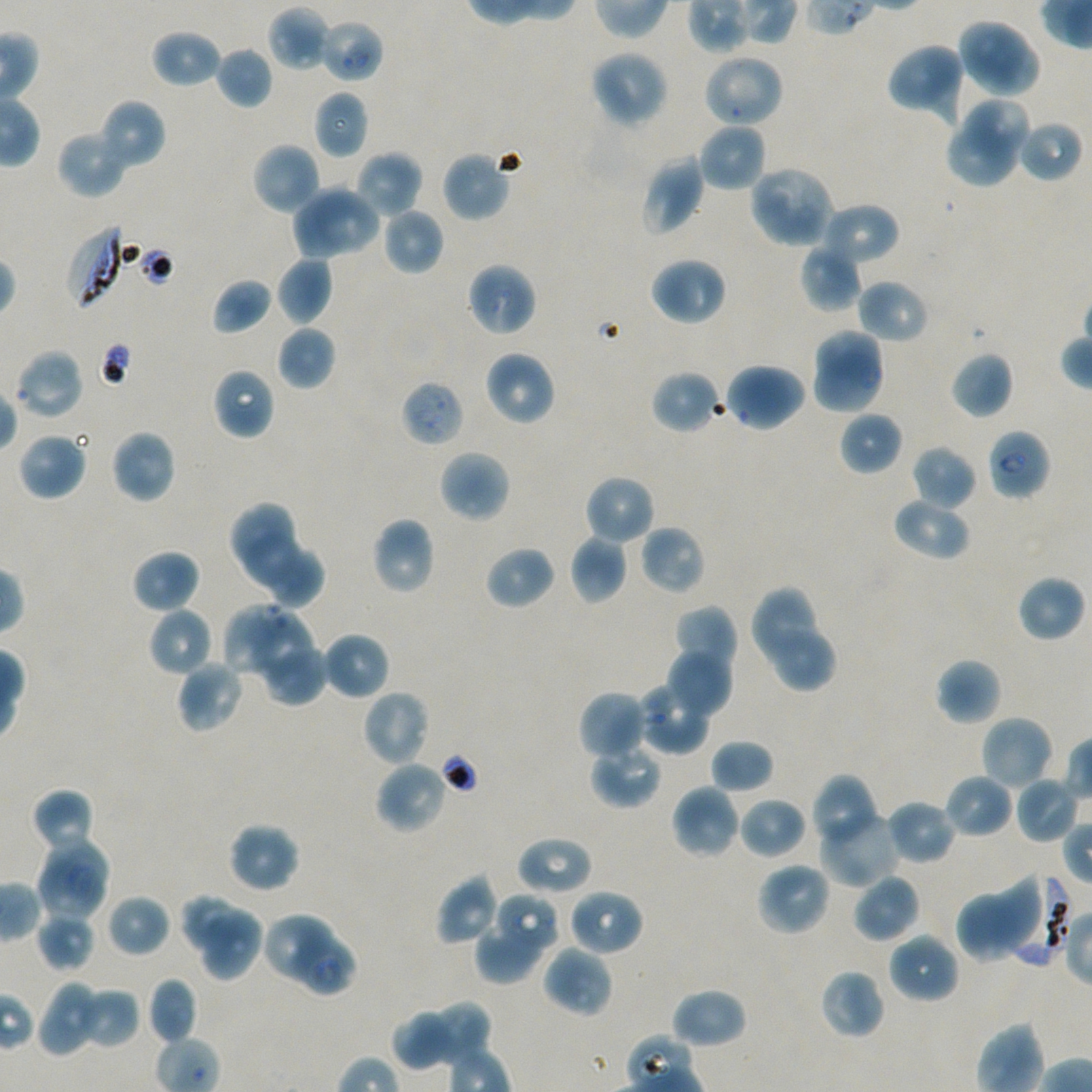
Approximate bounding rectangles given as corner coordinates in pixels from the top-left. Not every red blood cell is marked. A life-cycle stage — or a range of stages, where the recorded stages span more than one — follows each staged infected red blood cell.
Summary:
  - Locations of uninfected red blood cells: (x1=266, y1=6, x2=330, y2=72), (x1=957, y1=16, x2=1027, y2=88), (x1=150, y1=29, x2=221, y2=88), (x1=971, y1=37, x2=1038, y2=98), (x1=886, y1=42, x2=966, y2=121), (x1=215, y1=46, x2=273, y2=109), (x1=589, y1=49, x2=670, y2=129), (x1=701, y1=54, x2=785, y2=128), (x1=313, y1=90, x2=369, y2=160), (x1=98, y1=98, x2=166, y2=170), (x1=963, y1=102, x2=1030, y2=158), (x1=1016, y1=120, x2=1083, y2=184), (x1=697, y1=122, x2=767, y2=192), (x1=947, y1=126, x2=1017, y2=187), (x1=56, y1=129, x2=131, y2=199), (x1=252, y1=142, x2=321, y2=216), (x1=441, y1=150, x2=512, y2=222), (x1=354, y1=151, x2=422, y2=219), (x1=640, y1=154, x2=705, y2=236), (x1=748, y1=164, x2=836, y2=249), (x1=295, y1=179, x2=354, y2=260), (x1=315, y1=185, x2=382, y2=253), (x1=818, y1=202, x2=900, y2=268), (x1=381, y1=207, x2=444, y2=275), (x1=800, y1=240, x2=863, y2=312), (x1=276, y1=255, x2=333, y2=326), (x1=649, y1=256, x2=728, y2=326), (x1=467, y1=261, x2=537, y2=338), (x1=212, y1=278, x2=272, y2=335), (x1=856, y1=278, x2=930, y2=344), (x1=276, y1=325, x2=336, y2=390), (x1=813, y1=329, x2=883, y2=384), (x1=14, y1=348, x2=84, y2=420), (x1=483, y1=350, x2=556, y2=426), (x1=812, y1=350, x2=886, y2=416), (x1=950, y1=351, x2=1013, y2=419), (x1=724, y1=362, x2=807, y2=433), (x1=212, y1=367, x2=275, y2=441), (x1=651, y1=369, x2=724, y2=434), (x1=839, y1=410, x2=903, y2=476), (x1=110, y1=428, x2=177, y2=503), (x1=17, y1=431, x2=89, y2=501), (x1=912, y1=445, x2=977, y2=510), (x1=438, y1=449, x2=511, y2=523), (x1=583, y1=474, x2=655, y2=545), (x1=892, y1=496, x2=972, y2=560), (x1=228, y1=503, x2=293, y2=564), (x1=371, y1=516, x2=437, y2=595), (x1=639, y1=525, x2=706, y2=596), (x1=242, y1=531, x2=304, y2=587), (x1=569, y1=534, x2=629, y2=604), (x1=485, y1=545, x2=556, y2=609), (x1=131, y1=548, x2=202, y2=613), (x1=271, y1=549, x2=325, y2=611), (x1=1016, y1=575, x2=1085, y2=642), (x1=749, y1=586, x2=817, y2=663), (x1=223, y1=604, x2=286, y2=674), (x1=673, y1=604, x2=738, y2=672), (x1=147, y1=606, x2=214, y2=677), (x1=255, y1=613, x2=314, y2=679), (x1=322, y1=631, x2=390, y2=699), (x1=776, y1=632, x2=837, y2=689), (x1=666, y1=647, x2=732, y2=718), (x1=266, y1=648, x2=328, y2=706), (x1=935, y1=657, x2=1002, y2=725), (x1=175, y1=659, x2=245, y2=734), (x1=637, y1=684, x2=711, y2=755), (x1=361, y1=689, x2=431, y2=767), (x1=577, y1=689, x2=649, y2=762), (x1=980, y1=715, x2=1055, y2=792), (x1=710, y1=739, x2=774, y2=793), (x1=593, y1=746, x2=660, y2=807), (x1=374, y1=760, x2=449, y2=835), (x1=810, y1=774, x2=873, y2=840), (x1=943, y1=774, x2=1014, y2=839), (x1=1015, y1=775, x2=1078, y2=843), (x1=670, y1=784, x2=741, y2=860), (x1=31, y1=788, x2=96, y2=856), (x1=739, y1=797, x2=808, y2=860), (x1=885, y1=799, x2=958, y2=864), (x1=820, y1=807, x2=900, y2=887), (x1=228, y1=821, x2=300, y2=893), (x1=46, y1=835, x2=107, y2=899), (x1=516, y1=835, x2=594, y2=896), (x1=756, y1=862, x2=832, y2=937), (x1=36, y1=864, x2=107, y2=922), (x1=852, y1=873, x2=922, y2=943), (x1=435, y1=874, x2=500, y2=946), (x1=956, y1=877, x2=1044, y2=962), (x1=568, y1=888, x2=644, y2=956), (x1=107, y1=894, x2=171, y2=957), (x1=500, y1=896, x2=557, y2=947), (x1=182, y1=897, x2=249, y2=949), (x1=200, y1=908, x2=260, y2=982), (x1=36, y1=913, x2=95, y2=971), (x1=267, y1=916, x2=333, y2=979), (x1=479, y1=922, x2=542, y2=983), (x1=888, y1=932, x2=960, y2=1004), (x1=289, y1=936, x2=358, y2=996), (x1=543, y1=945, x2=613, y2=1017), (x1=819, y1=968, x2=885, y2=1039), (x1=147, y1=977, x2=198, y2=1045), (x1=37, y1=979, x2=103, y2=1057), (x1=79, y1=987, x2=139, y2=1049), (x1=670, y1=987, x2=748, y2=1049), (x1=435, y1=998, x2=490, y2=1070), (x1=392, y1=1011, x2=448, y2=1072)
  - Locations of red blood cells of indeterminate infection status: (x1=318, y1=18, x2=384, y2=83), (x1=401, y1=380, x2=464, y2=447)
  - Locations of infected red blood cells: (x1=67, y1=225, x2=131, y2=309); (x1=987, y1=428, x2=1051, y2=500) early ring to early trophozoite; (x1=1011, y1=875, x2=1075, y2=966)
  - Culture: static in-vitro P. falciparum strain NF54
  - Stain: Giemsa
  - Field of view: single
  - Donor blood group: A+/O+
  - Objective: 100x, oil immersion, numerical aperture 1.45
  - Preparation: thin blood film
  - Image size: 1092×1092 pixels